Locate every Plasmodium ovale-infected red blood cell.
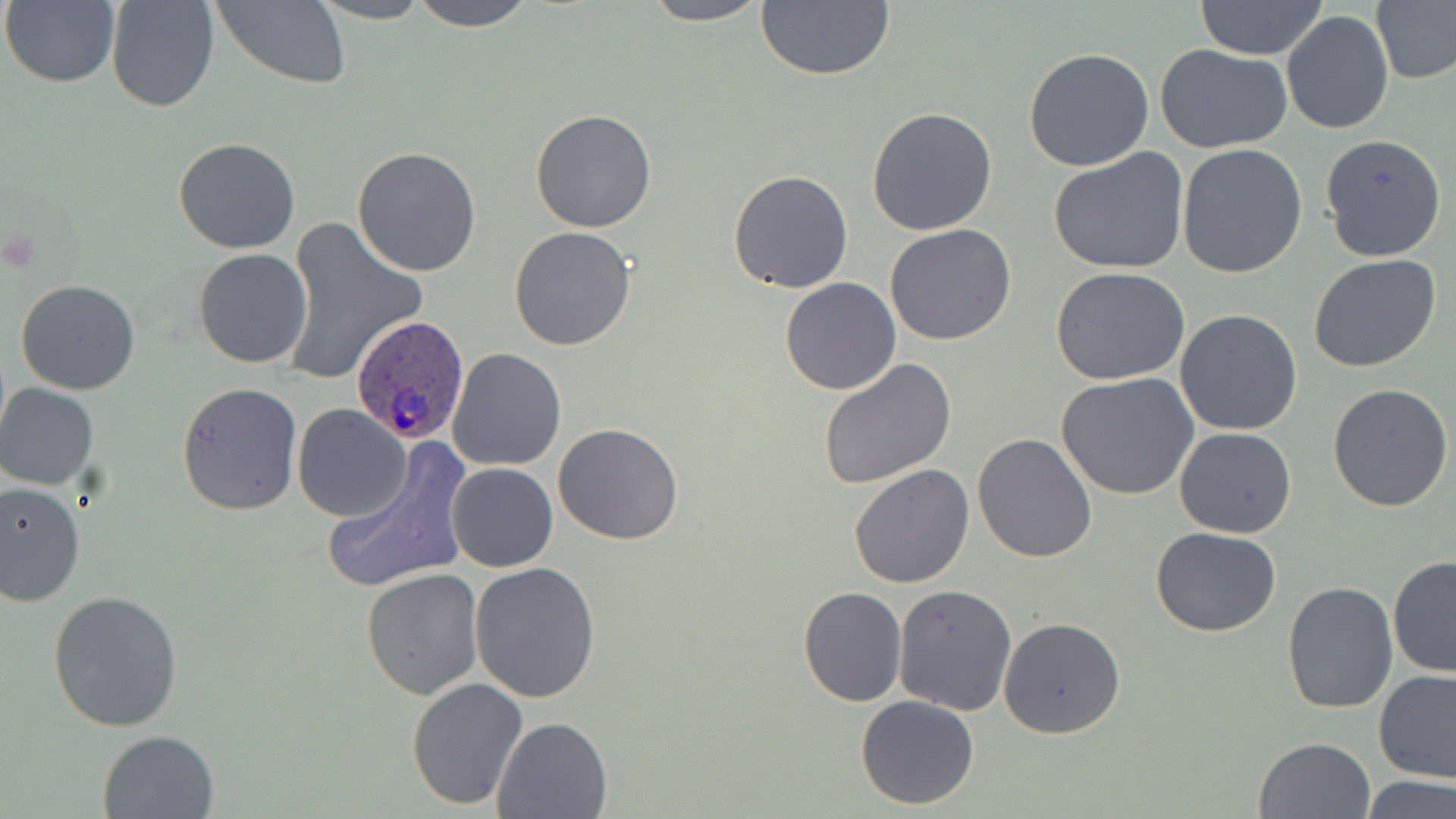

Approximate bounding boxes as [x1, y1, x2, y2] in pixels.
Plasmodium ovale-infected red blood cells: [350, 315, 469, 444].

{
  "slide_level_diagnosis": "Plasmodium ovale",
  "field_of_view": "single",
  "stain": "May-Grünwald-Giemsa",
  "image_size": "1456×819 pixels",
  "modality": "optical microscopy",
  "uninfected_red_blood_cell_locations": "approximate bounding boxes as [x1, y1, x2, y2] in pixels: [2, 0, 121, 88], [106, 0, 219, 112], [213, 0, 350, 89], [310, 0, 435, 25], [410, 0, 536, 30], [637, 0, 773, 26], [755, 0, 896, 81], [1373, 0, 1456, 86], [1195, 1, 1329, 60], [1282, 10, 1392, 135], [1156, 44, 1293, 155], [1023, 47, 1154, 172], [866, 106, 998, 234], [531, 108, 657, 232], [1319, 134, 1447, 263], [173, 137, 299, 254], [1178, 145, 1307, 281], [352, 146, 481, 277], [1046, 149, 1190, 277], [729, 171, 854, 293], [280, 216, 429, 387], [884, 224, 1016, 347], [510, 227, 637, 349], [192, 248, 312, 368], [1308, 253, 1441, 373], [1049, 268, 1191, 386], [779, 277, 901, 396], [16, 280, 141, 395], [1174, 308, 1302, 436], [445, 347, 566, 471], [818, 357, 956, 488], [1057, 374, 1200, 502], [177, 381, 303, 515], [1, 384, 99, 491], [1328, 384, 1454, 512], [293, 405, 411, 521], [553, 422, 682, 545], [1173, 427, 1296, 538], [973, 433, 1097, 563], [321, 449, 470, 595], [446, 462, 558, 572], [848, 463, 976, 590], [0, 482, 85, 605], [1152, 526, 1279, 637], [1388, 556, 1456, 677], [469, 562, 601, 704], [361, 567, 486, 701], [1282, 581, 1399, 716], [894, 585, 1017, 716], [798, 586, 907, 706], [47, 587, 187, 731], [999, 616, 1126, 740], [1372, 670, 1456, 784], [406, 678, 526, 811], [856, 695, 981, 808], [493, 716, 613, 817], [97, 729, 220, 819], [1254, 736, 1377, 819], [1359, 775, 1454, 819]",
  "preparation": "thin blood film",
  "magnification": "1000x"
}